Identify the blood parasite species.
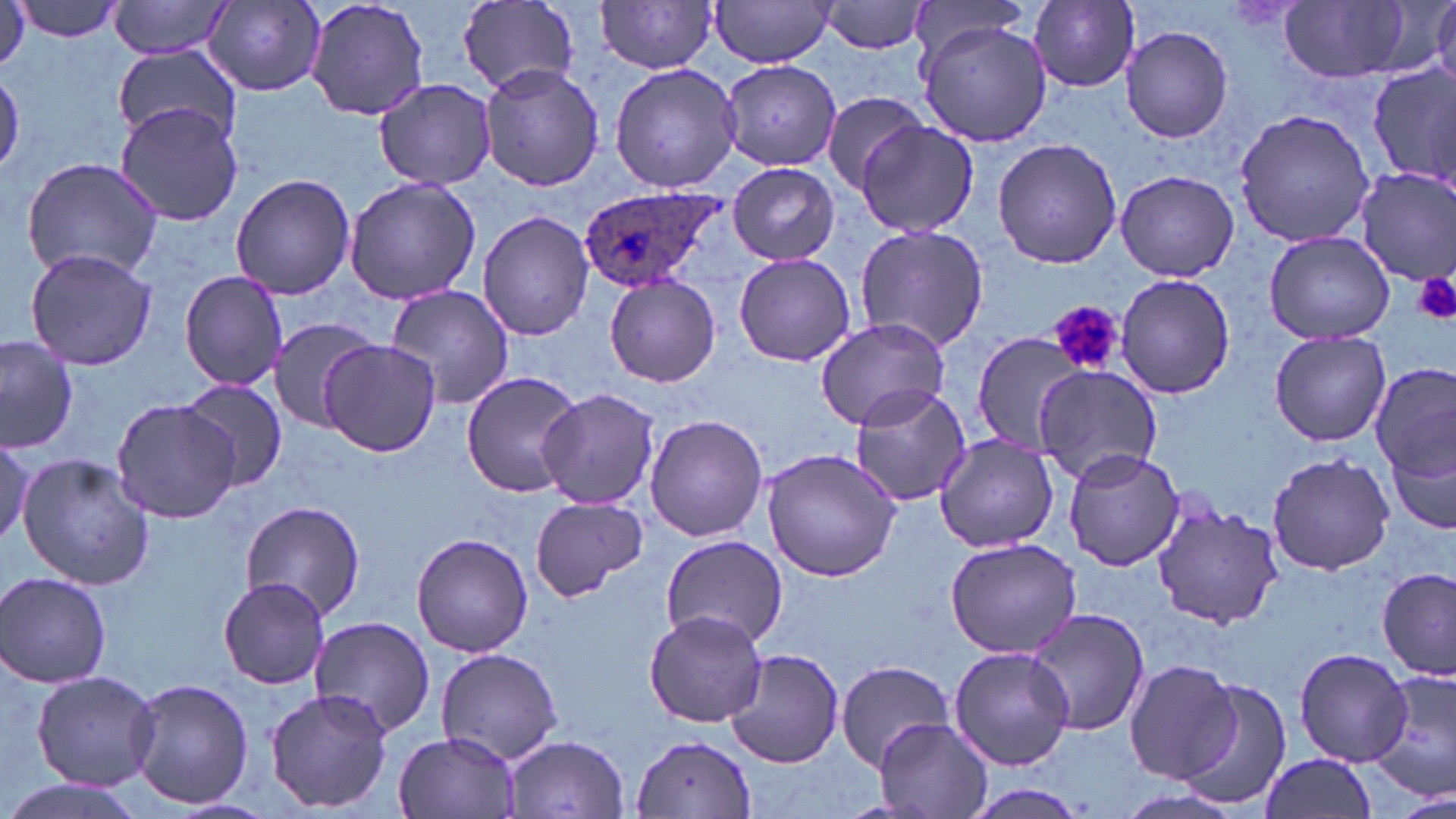

Plasmodium ovale.

Summary:
  - Coordinate format: approximate bounding boxes as (x1, y1, x2, y2) in pixels
  - Platelet locations: (1413, 271, 1456, 323), (1051, 299, 1125, 378)
  - Uninfected red blood cell locations: (0, 0, 29, 78), (14, 0, 124, 40), (110, 0, 233, 58), (302, 0, 430, 121), (710, 0, 837, 67), (457, 1, 581, 99), (821, 1, 934, 55), (1029, 1, 1139, 90), (1280, 1, 1414, 83), (201, 2, 327, 94), (596, 2, 722, 74), (910, 2, 1035, 69), (1431, 3, 1456, 92), (919, 21, 1053, 148), (1120, 25, 1234, 143), (113, 45, 243, 147), (720, 60, 844, 169), (609, 62, 743, 194), (478, 63, 604, 191), (1365, 64, 1455, 191), (1, 70, 24, 175), (374, 77, 498, 190), (820, 91, 927, 193), (115, 102, 243, 227), (1233, 107, 1376, 248), (855, 120, 980, 239), (992, 137, 1123, 269), (22, 157, 162, 282), (729, 163, 839, 265), (1355, 167, 1456, 287), (1114, 169, 1240, 281), (230, 173, 357, 298), (344, 175, 480, 305), (477, 210, 593, 341), (853, 224, 990, 353), (1264, 231, 1396, 345), (26, 248, 157, 373), (734, 252, 855, 366), (179, 271, 290, 391), (1116, 274, 1236, 399), (604, 275, 720, 389), (383, 285, 515, 408), (266, 316, 378, 431), (814, 316, 952, 431), (972, 330, 1089, 455), (1270, 330, 1391, 447), (0, 334, 78, 454), (319, 339, 441, 456), (1033, 364, 1164, 482), (1373, 366, 1453, 486), (461, 371, 586, 498), (177, 377, 287, 493), (848, 386, 973, 507), (538, 389, 661, 508), (113, 396, 240, 524), (645, 414, 769, 541), (1, 437, 35, 545), (936, 437, 1059, 553), (1387, 441, 1455, 539), (760, 447, 903, 581), (1061, 449, 1185, 571), (1265, 452, 1395, 575), (16, 453, 154, 592), (530, 498, 650, 599), (238, 499, 367, 623), (1151, 499, 1286, 632), (412, 532, 534, 658), (659, 537, 789, 649), (943, 537, 1082, 659), (1377, 568, 1452, 679), (2, 572, 113, 688), (217, 576, 332, 689), (644, 609, 768, 728), (1023, 609, 1149, 736), (307, 616, 437, 737), (948, 645, 1074, 771), (435, 646, 564, 766), (1294, 647, 1415, 768), (726, 648, 844, 768), (1124, 659, 1243, 784), (835, 660, 955, 770), (1370, 667, 1456, 799), (30, 668, 160, 790), (1180, 677, 1294, 811), (126, 679, 254, 811), (264, 687, 395, 813), (875, 718, 993, 818), (393, 731, 519, 818), (505, 734, 628, 817), (631, 735, 758, 819), (1256, 752, 1379, 819), (0, 779, 146, 819), (963, 782, 1094, 819), (1395, 793, 1455, 819)
  - Plasmodium ovale-infected red blood cell locations: (577, 188, 730, 296)
  - Image size: 1456×819 pixels
  - Preparation: thin blood film
  - Field of view: single
  - Magnification: 1000x
  - Stain: May-Grünwald-Giemsa
  - Modality: light microscopy